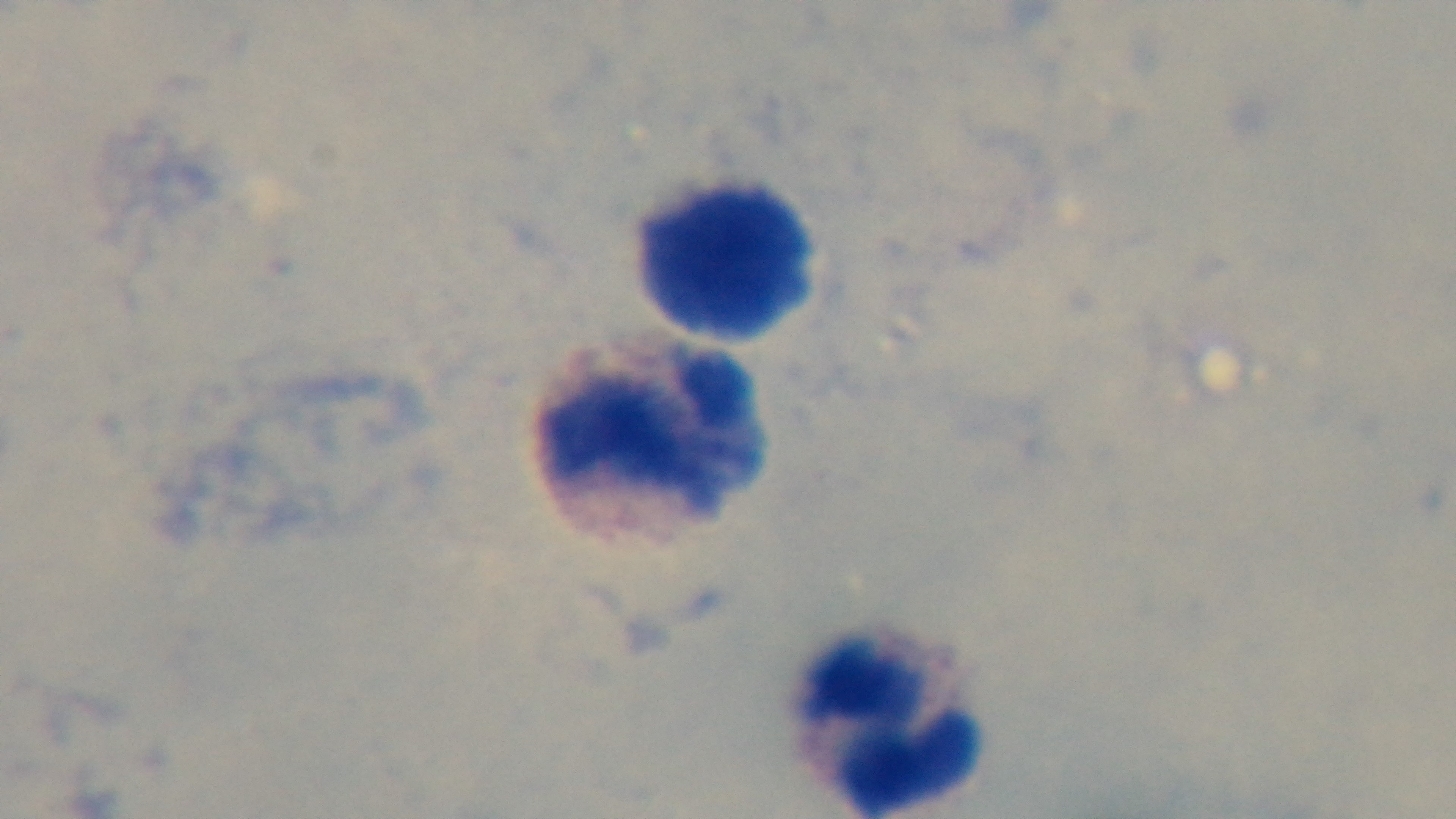
Summary:
  - Malaria status: uninfected
  - Modality: light microscopy
  - Field of view: single
  - Capture: mounted 4K digital camera
  - Preparation: thick blood film
  - Stain: Giemsa
  - Objective: 100x oil immersion